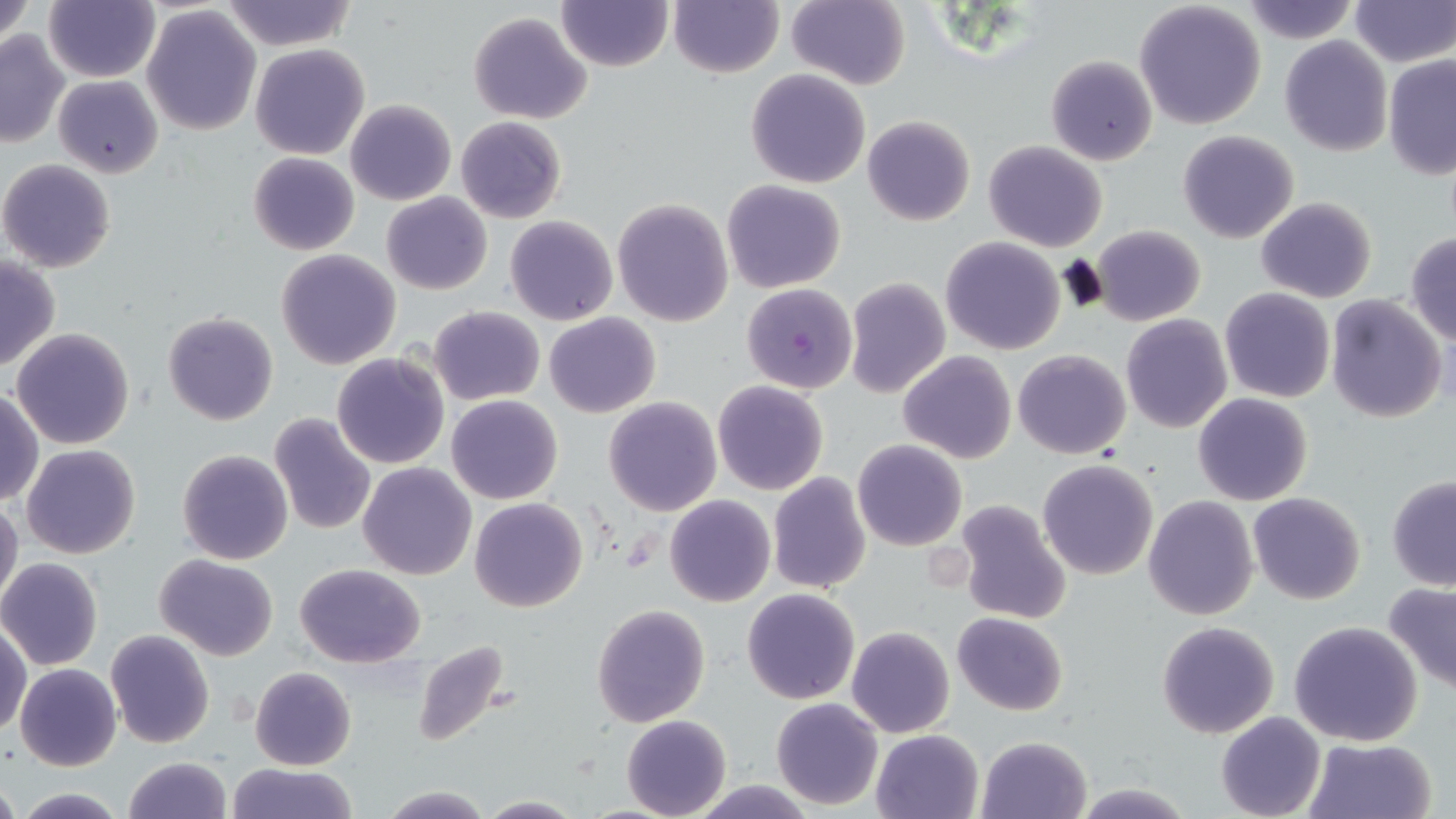 Approximate bounding boxes as (x1, y1, x2, y2) in pixels. Uninfected red blood cell locations: (1, 0, 34, 59), (45, 0, 158, 82), (668, 0, 783, 77), (785, 0, 910, 89), (1349, 0, 1453, 67), (223, 1, 356, 50), (555, 1, 673, 72), (1133, 2, 1268, 130), (1239, 2, 1361, 45), (142, 4, 263, 136), (468, 11, 593, 125), (0, 31, 70, 148), (1279, 36, 1392, 156), (250, 43, 369, 160), (1046, 54, 1157, 166), (1382, 55, 1455, 176), (746, 68, 870, 188), (53, 75, 163, 180), (345, 99, 456, 205), (862, 115, 975, 226), (455, 117, 567, 223), (1177, 131, 1300, 244), (984, 141, 1108, 253), (250, 152, 358, 255), (0, 158, 117, 272), (722, 179, 847, 294), (380, 191, 492, 295), (1256, 197, 1378, 304), (612, 199, 733, 327), (505, 215, 617, 325), (1091, 225, 1206, 327), (1405, 231, 1456, 346), (939, 236, 1066, 355), (274, 249, 400, 369), (0, 255, 61, 374), (844, 277, 950, 398), (1219, 288, 1335, 403), (1326, 295, 1448, 423), (428, 306, 545, 405), (162, 313, 279, 426), (544, 313, 661, 419), (1120, 315, 1233, 434), (11, 327, 135, 449), (1013, 349, 1131, 459), (898, 351, 1016, 462), (332, 353, 451, 470), (712, 380, 828, 495), (1, 389, 43, 506), (1193, 392, 1313, 505), (447, 395, 563, 504), (602, 397, 722, 516), (268, 412, 376, 536), (852, 440, 967, 551), (22, 445, 140, 560), (177, 449, 293, 566), (1038, 459, 1159, 581), (358, 462, 477, 580), (767, 471, 871, 594), (1387, 474, 1456, 591), (1248, 492, 1366, 605), (665, 494, 776, 607), (1143, 496, 1258, 621), (0, 497, 23, 613), (468, 497, 587, 612), (951, 499, 1072, 625), (153, 554, 280, 660), (0, 557, 103, 670), (295, 562, 425, 667), (1383, 581, 1456, 695), (742, 588, 860, 705), (591, 603, 710, 728), (952, 611, 1067, 715), (1, 620, 30, 736), (1156, 620, 1279, 738), (1288, 620, 1423, 747), (846, 625, 955, 738), (105, 630, 214, 748), (411, 639, 515, 750), (15, 662, 122, 771), (250, 666, 357, 770), (770, 696, 883, 810), (1215, 712, 1325, 819), (622, 715, 731, 819), (871, 729, 984, 818), (977, 735, 1091, 818), (1303, 737, 1437, 819), (122, 756, 232, 819), (223, 762, 361, 819), (0, 778, 21, 819), (689, 779, 818, 817), (1070, 781, 1193, 818), (379, 785, 492, 818), (13, 789, 131, 819), (475, 795, 585, 817). Plasmodium falciparum-infected red blood cell locations: (741, 283, 858, 393). Slide-level diagnosis: Plasmodium falciparum. Light microscopy. Thin blood smear. 1000x magnification. Image is 1456×819 pixels. May-Grünwald-Giemsa stain. Single field of view.